Outline each blood parasite and name the species.
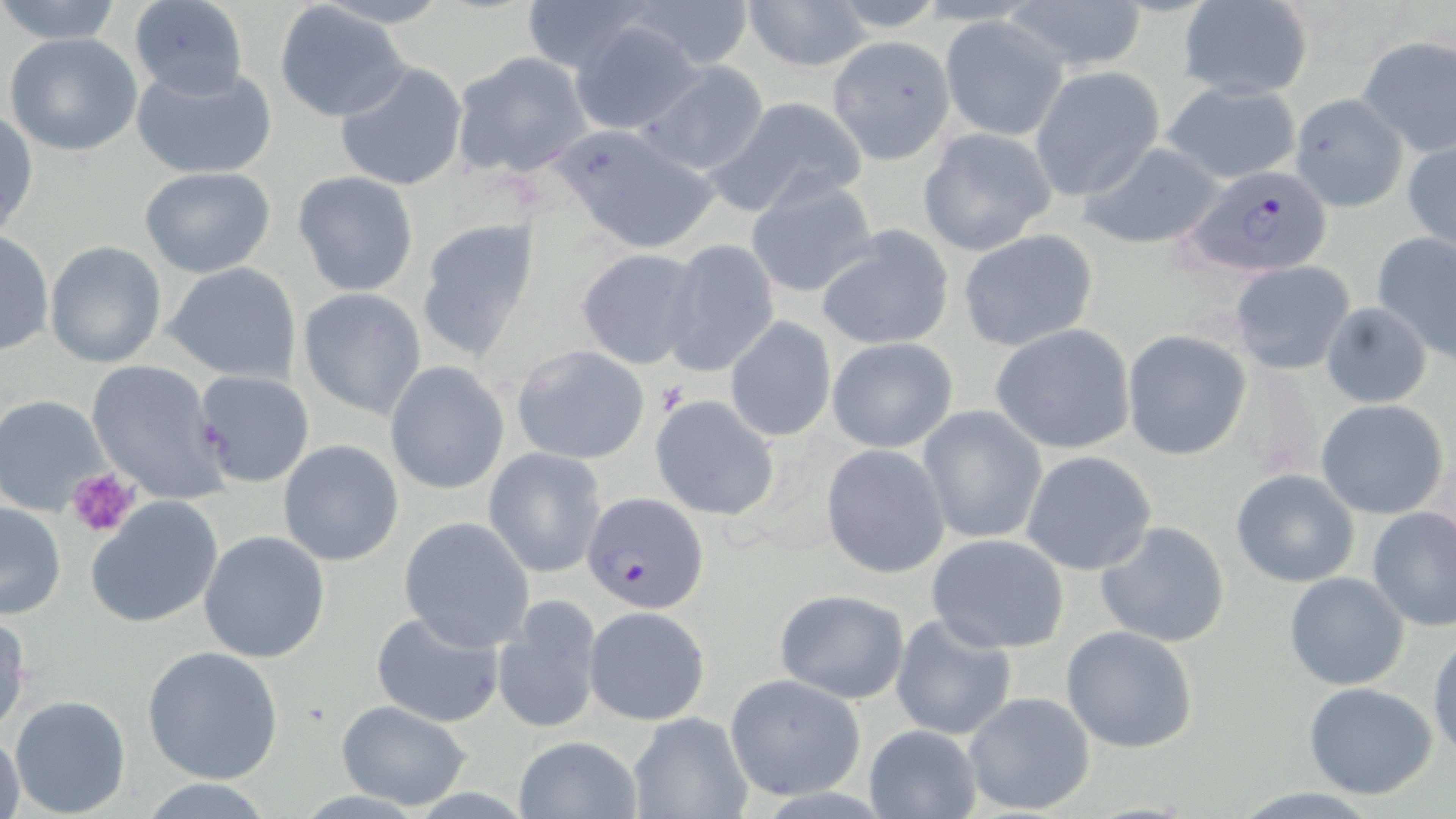
Approximate bounding boxes as named x1/y1/x2/y2 corners in pixels.
Plasmodium falciparum-infected red blood cells: (x1=1180, y1=165, x2=1337, y2=278), (x1=581, y1=490, x2=710, y2=615).
No Plasmodium ovale, Plasmodium malariae, Plasmodium vivax, Babesia divergens, or Trypanosoma brucei observed.

Uninfected red blood cell locations: (x1=518, y1=0, x2=658, y2=77), (x1=616, y1=0, x2=759, y2=70), (x1=739, y1=0, x2=877, y2=72), (x1=1004, y1=0, x2=1150, y2=73), (x1=0, y1=1, x2=128, y2=47), (x1=1174, y1=1, x2=1315, y2=99), (x1=127, y1=3, x2=249, y2=99), (x1=275, y1=5, x2=409, y2=123), (x1=939, y1=16, x2=1070, y2=142), (x1=569, y1=21, x2=705, y2=136), (x1=4, y1=33, x2=142, y2=156), (x1=1356, y1=34, x2=1456, y2=158), (x1=828, y1=36, x2=957, y2=163), (x1=450, y1=52, x2=593, y2=179), (x1=637, y1=58, x2=770, y2=177), (x1=131, y1=61, x2=277, y2=180), (x1=334, y1=63, x2=469, y2=192), (x1=1029, y1=66, x2=1165, y2=200), (x1=1161, y1=80, x2=1303, y2=186), (x1=1290, y1=92, x2=1408, y2=212), (x1=708, y1=95, x2=869, y2=218), (x1=1, y1=109, x2=38, y2=240), (x1=551, y1=124, x2=721, y2=254), (x1=917, y1=127, x2=1058, y2=255), (x1=1402, y1=138, x2=1456, y2=252), (x1=1078, y1=141, x2=1231, y2=250), (x1=138, y1=166, x2=276, y2=278), (x1=292, y1=171, x2=420, y2=296), (x1=744, y1=178, x2=879, y2=300), (x1=414, y1=215, x2=544, y2=361), (x1=816, y1=226, x2=955, y2=352), (x1=957, y1=228, x2=1098, y2=353), (x1=0, y1=230, x2=53, y2=358), (x1=1372, y1=231, x2=1456, y2=358), (x1=658, y1=239, x2=781, y2=379), (x1=44, y1=240, x2=167, y2=369), (x1=576, y1=249, x2=704, y2=371), (x1=1230, y1=260, x2=1356, y2=375), (x1=164, y1=262, x2=302, y2=384), (x1=297, y1=288, x2=428, y2=420), (x1=1320, y1=302, x2=1433, y2=407), (x1=723, y1=316, x2=838, y2=442), (x1=989, y1=324, x2=1137, y2=455), (x1=1122, y1=331, x2=1252, y2=460), (x1=826, y1=337, x2=958, y2=453), (x1=512, y1=344, x2=650, y2=464), (x1=85, y1=360, x2=228, y2=503), (x1=384, y1=361, x2=509, y2=494), (x1=1225, y1=364, x2=1328, y2=482), (x1=191, y1=367, x2=316, y2=490), (x1=0, y1=394, x2=112, y2=517), (x1=649, y1=394, x2=780, y2=522), (x1=1315, y1=399, x2=1450, y2=520), (x1=916, y1=405, x2=1049, y2=544), (x1=277, y1=439, x2=405, y2=567), (x1=820, y1=444, x2=951, y2=578), (x1=484, y1=447, x2=608, y2=578), (x1=1021, y1=450, x2=1159, y2=576), (x1=1231, y1=470, x2=1360, y2=587), (x1=86, y1=496, x2=224, y2=628), (x1=0, y1=502, x2=67, y2=621), (x1=1368, y1=506, x2=1456, y2=630), (x1=398, y1=516, x2=535, y2=650), (x1=1094, y1=520, x2=1232, y2=648), (x1=197, y1=529, x2=332, y2=665), (x1=927, y1=533, x2=1069, y2=652), (x1=1284, y1=572, x2=1411, y2=691), (x1=774, y1=588, x2=910, y2=703), (x1=494, y1=596, x2=602, y2=734), (x1=582, y1=605, x2=711, y2=725), (x1=369, y1=609, x2=504, y2=729), (x1=0, y1=613, x2=30, y2=738), (x1=889, y1=614, x2=1018, y2=742), (x1=1060, y1=625, x2=1200, y2=754), (x1=1428, y1=636, x2=1456, y2=761), (x1=142, y1=645, x2=284, y2=783), (x1=723, y1=673, x2=864, y2=800), (x1=1302, y1=682, x2=1439, y2=799), (x1=961, y1=691, x2=1097, y2=813), (x1=7, y1=695, x2=132, y2=817), (x1=335, y1=700, x2=474, y2=811), (x1=627, y1=712, x2=752, y2=819), (x1=865, y1=726, x2=981, y2=818), (x1=0, y1=732, x2=27, y2=818), (x1=513, y1=735, x2=642, y2=818), (x1=138, y1=779, x2=276, y2=817). Platelet locations: (x1=66, y1=467, x2=139, y2=538). Slide-level diagnosis: Plasmodium falciparum. Light microscopy. Thin blood film. May-Grünwald-Giemsa-stained preparation. 1000x magnification. Single field of view. Image is 1456×819 pixels.